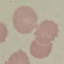
Summary:
  - Result: negative for malaria parasites
  - Image type: automatically extracted cell patch, resized to 64 × 64 pixels
  - Stain: Giemsa
  - Capture: smartphone through the microscope eyepiece
  - Preparation: thin smear